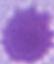
Captured at 1000x magnification. Photomicrograph. A red blood cell is shown.